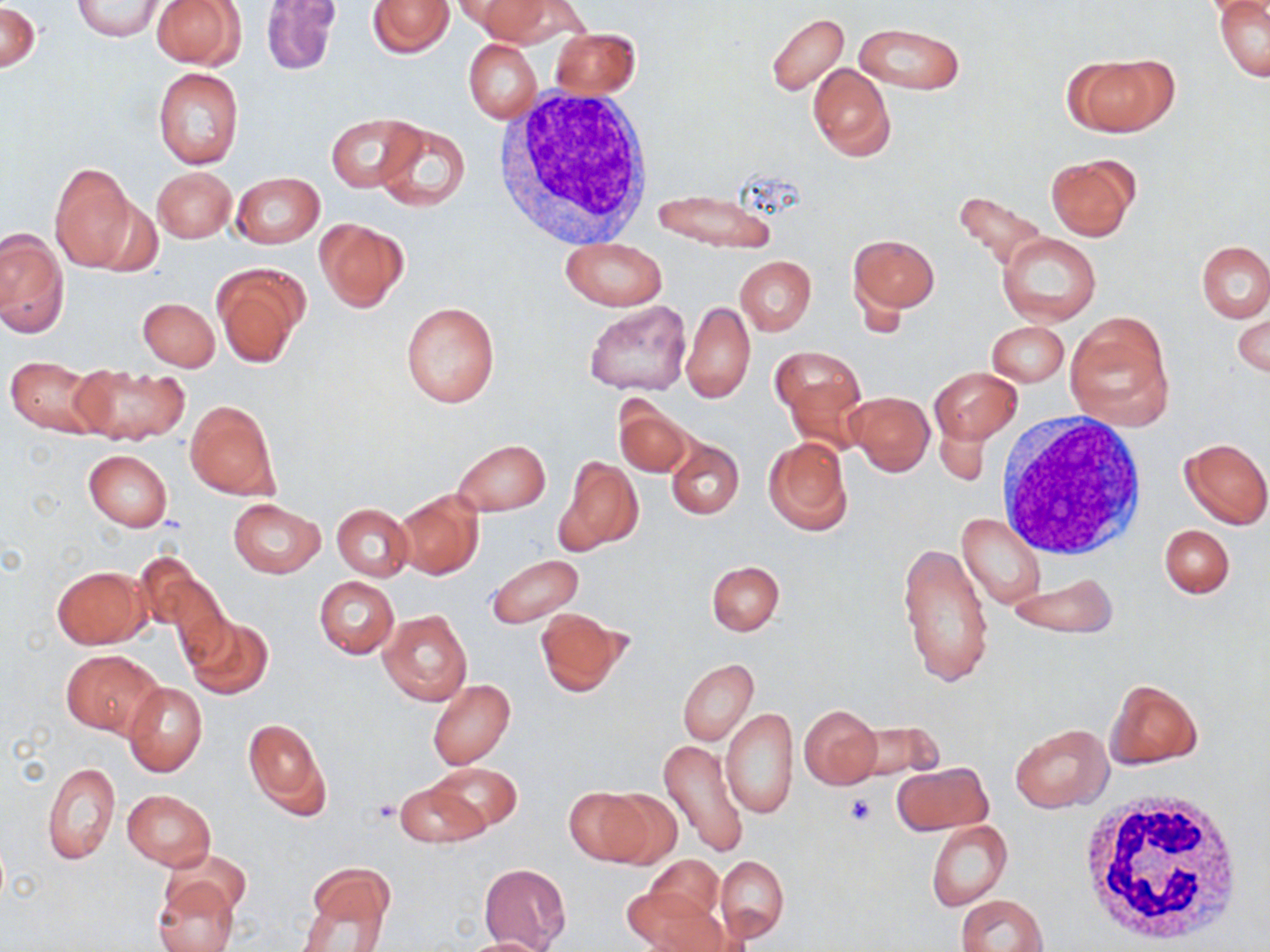
slide-level diagnosis = no evidence of blood parasites
modality = optical microscopy
platelet locations = approximate bounding boxes as (x1, y1, x2, y2) in pixels: (845, 793, 876, 826), (371, 799, 400, 824)
preparation = thin blood smear
uninfected red blood cell locations = approximate bounding boxes as (x1, y1, x2, y2) in pixels: (72, 0, 164, 40), (258, 0, 340, 74), (367, 0, 452, 58), (461, 0, 552, 40), (150, 1, 245, 69), (1214, 1, 1270, 81), (0, 3, 41, 73), (764, 13, 848, 98), (854, 22, 965, 95), (551, 28, 640, 97), (464, 40, 542, 124), (1068, 55, 1174, 135), (807, 63, 895, 162), (151, 68, 245, 170), (325, 114, 421, 193), (373, 120, 472, 213), (1046, 155, 1138, 240), (49, 163, 138, 272), (153, 166, 236, 243), (231, 172, 325, 248), (653, 188, 778, 253), (951, 189, 1051, 273), (315, 218, 408, 311), (0, 228, 67, 337), (997, 233, 1101, 326), (850, 235, 939, 314), (562, 238, 666, 311), (1197, 241, 1269, 321), (734, 256, 815, 336), (213, 264, 307, 367), (139, 297, 219, 371), (399, 300, 501, 408), (584, 300, 691, 396), (682, 301, 755, 403), (1231, 303, 1270, 379), (1066, 313, 1173, 426), (986, 320, 1069, 386), (770, 346, 864, 426), (3, 356, 110, 438), (73, 363, 190, 446), (929, 366, 1021, 443), (848, 391, 934, 476), (185, 399, 278, 500), (614, 399, 695, 479), (763, 437, 852, 535), (1180, 437, 1270, 528), (666, 438, 743, 518), (453, 440, 551, 515), (83, 449, 172, 530), (555, 457, 642, 555), (393, 489, 485, 580), (228, 498, 325, 578), (332, 504, 412, 582), (958, 514, 1046, 610), (1159, 523, 1236, 599), (898, 538, 995, 689), (135, 554, 226, 648), (487, 554, 583, 628), (706, 561, 784, 635), (51, 565, 149, 648), (1011, 576, 1116, 640), (314, 577, 399, 658), (535, 608, 629, 696), (378, 609, 472, 706), (183, 616, 274, 701), (61, 649, 163, 736), (677, 659, 758, 744), (427, 679, 516, 770), (1104, 679, 1202, 768), (123, 683, 207, 776), (799, 705, 881, 789), (721, 708, 798, 819), (242, 718, 329, 818), (851, 720, 947, 784), (1010, 723, 1112, 813), (657, 739, 751, 860), (42, 762, 119, 865), (426, 762, 522, 834), (892, 762, 991, 836), (394, 780, 487, 849), (564, 786, 654, 865), (598, 786, 682, 871), (122, 788, 215, 870), (926, 820, 1012, 912), (163, 849, 252, 918), (647, 855, 725, 926), (715, 855, 788, 943), (301, 864, 395, 945), (479, 864, 570, 950), (152, 874, 239, 952), (625, 885, 722, 952), (956, 893, 1047, 952), (458, 936, 553, 952)
stain = May-Grünwald-Giemsa
white blood cell locations = approximate bounding boxes as (x1, y1, x2, y2) in pixels: (495, 90, 658, 247), (994, 417, 1147, 563), (1076, 789, 1248, 949)
magnification = 1000x
field of view = one of a larger specimen
image size = 1270×952 pixels